Report the malaria status of this cell.
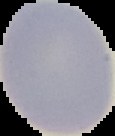
Uninfected.

{
  "image_type": "cell region segmented out of the field of view; surrounding area masked to black",
  "image_size": "115×136 pixels",
  "preparation": "thin blood smear"
}